Locate every Plasmodium malariae-infected red blood cell.
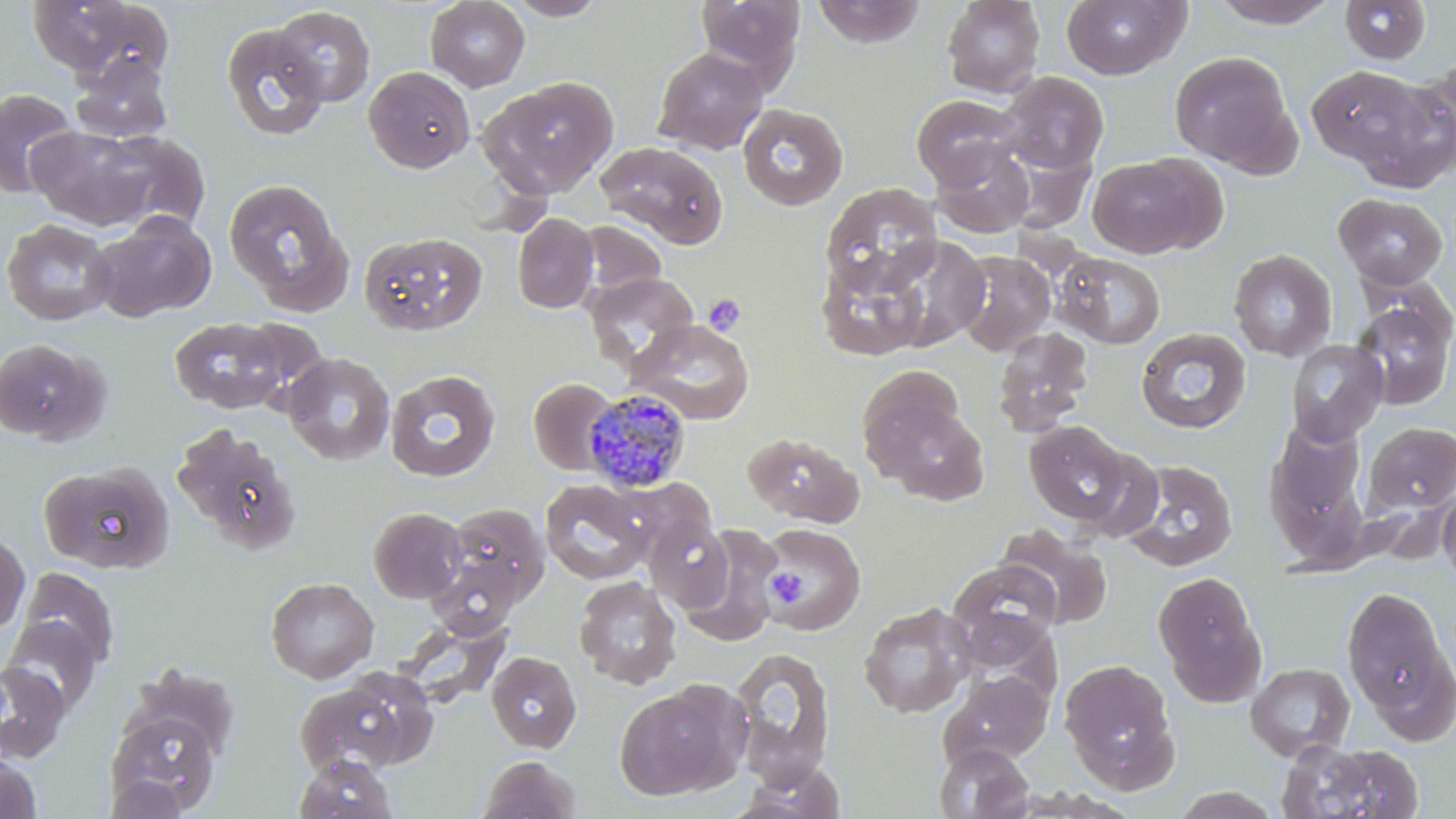

Approximate bounding boxes as (x1, y1, x2, y2) in pixels.
Plasmodium malariae-infected red blood cells: (583, 388, 692, 492).

Uninfected red blood cell locations: (425, 0, 530, 91), (505, 0, 609, 21), (694, 0, 806, 90), (941, 0, 1046, 99), (1059, 0, 1191, 80), (1208, 0, 1341, 28), (26, 1, 170, 84), (811, 1, 928, 47), (1340, 1, 1431, 66), (271, 5, 375, 107), (221, 23, 329, 142), (652, 46, 768, 155), (1170, 51, 1296, 172), (69, 53, 173, 144), (1415, 60, 1456, 160), (363, 65, 475, 173), (1307, 65, 1426, 167), (998, 71, 1109, 174), (1349, 74, 1456, 191), (480, 76, 617, 199), (1, 88, 79, 197), (911, 94, 1024, 189), (737, 102, 848, 211), (27, 124, 159, 230), (93, 131, 211, 233), (596, 141, 729, 249), (931, 141, 1034, 237), (1086, 153, 1216, 258), (223, 178, 351, 313), (819, 183, 941, 297), (1333, 192, 1448, 288), (88, 213, 216, 323), (512, 213, 598, 313), (1, 218, 117, 325), (578, 221, 667, 301), (359, 231, 487, 337), (875, 233, 986, 348), (815, 249, 935, 363), (1229, 249, 1338, 361), (953, 250, 1057, 356), (1054, 252, 1165, 349), (584, 271, 700, 371), (1350, 295, 1456, 410), (168, 316, 292, 414), (228, 316, 333, 414), (626, 320, 754, 424), (992, 326, 1094, 436), (1135, 327, 1252, 434), (0, 338, 106, 445), (1286, 339, 1388, 445), (282, 353, 395, 466), (855, 365, 967, 475), (385, 369, 500, 482), (528, 378, 618, 475), (869, 394, 989, 505), (1263, 419, 1371, 567), (1023, 420, 1133, 525), (1362, 421, 1456, 516), (171, 422, 302, 555), (743, 431, 863, 527), (1069, 446, 1166, 544), (1117, 458, 1239, 571), (40, 461, 174, 573), (607, 476, 717, 567), (540, 480, 651, 584), (1437, 485, 1456, 588), (439, 502, 551, 613), (367, 506, 466, 603), (644, 514, 734, 610), (760, 522, 868, 635), (995, 523, 1113, 630), (677, 525, 784, 647), (0, 530, 30, 637), (948, 559, 1063, 659), (16, 567, 119, 672), (1152, 570, 1267, 706), (265, 577, 379, 683), (573, 577, 682, 690), (1341, 584, 1455, 740), (858, 601, 976, 718), (393, 613, 512, 710), (3, 618, 102, 716), (729, 647, 836, 786), (486, 651, 582, 752), (1059, 658, 1180, 792), (0, 661, 71, 763), (1245, 662, 1355, 761), (125, 663, 242, 763), (295, 667, 438, 775), (940, 670, 1053, 768), (614, 682, 746, 799), (106, 708, 222, 814), (1276, 738, 1422, 819), (933, 743, 1034, 819), (0, 751, 42, 817), (294, 754, 398, 819), (477, 755, 581, 819), (732, 761, 849, 818), (104, 773, 191, 818), (1168, 786, 1288, 819). Platelet locations: (703, 294, 746, 336), (765, 568, 805, 602). Slide-level diagnosis: Plasmodium malariae. May-Grünwald-Giemsa stain. One field of a larger specimen. Optical microscopy. Thin blood smear. Captured at 1000x magnification. Image is 1456×819 pixels.